Classify this cell by malaria status.
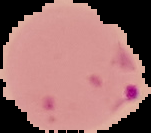
It is parasitized.

Summary:
  - Preparation: thin blood film
  - Image type: segmented cell region on a black background
  - Image size: 151×133 pixels